Point out each malaria parasite.
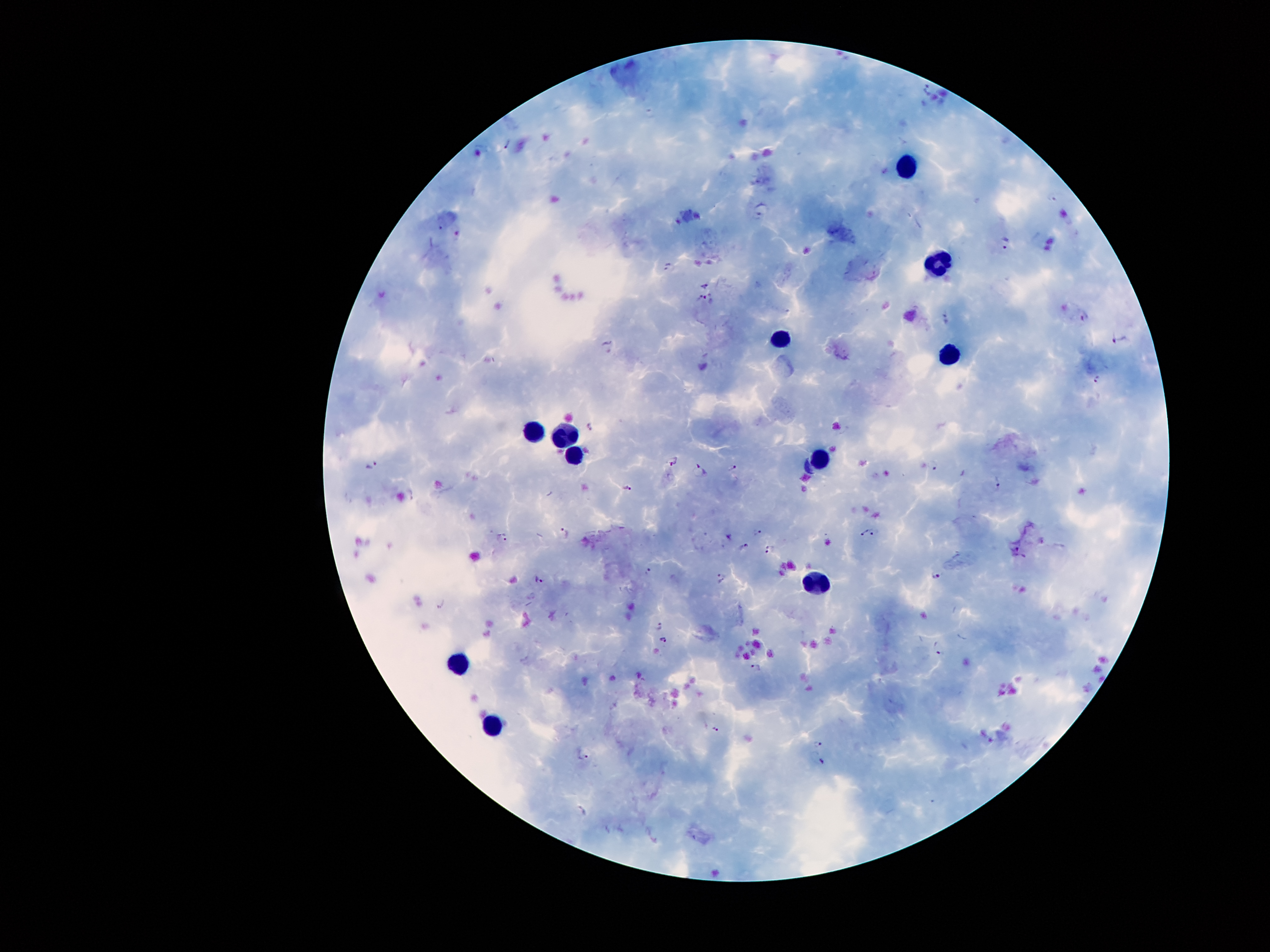

Approximate centers as (x, y) in pixels.
Malaria parasites: (930, 88), (506, 141), (762, 206), (442, 224), (1006, 244), (667, 267), (705, 284), (703, 299), (1083, 314), (944, 317), (1115, 340), (608, 343), (1097, 377), (590, 427), (672, 459), (373, 465), (935, 467), (734, 468), (701, 470), (998, 482), (629, 488), (409, 496), (758, 530), (876, 531), (564, 532), (864, 532), (730, 534), (504, 537), (744, 547), (771, 549), (1014, 550), (647, 571), (935, 573), (539, 579), (721, 579), (443, 603), (660, 623), (664, 639), (939, 648), (755, 668), (716, 729), (818, 744), (582, 754), (822, 762), (582, 810).

preparation: thick peripheral-blood smear
capture: smartphone through the microscope eyepiece
field_of_view: one from this slide
image_size: 1270×952 pixels
magnification: 100x
leukocyte_locations: 'approximate centers as (x, y) in pixels: (904, 164), (935, 262), (777, 333), (945, 354), (562, 430), (529, 432), (576, 456), (825, 460), (820, 583), (459, 662), (495, 725)'
stain: Giemsa
patient_malaria_status: positive for Plasmodium falciparum